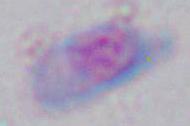

Summary:
  - Identification: Toxoplasma gondii
  - Modality: micrograph
  - Magnification: 1000x